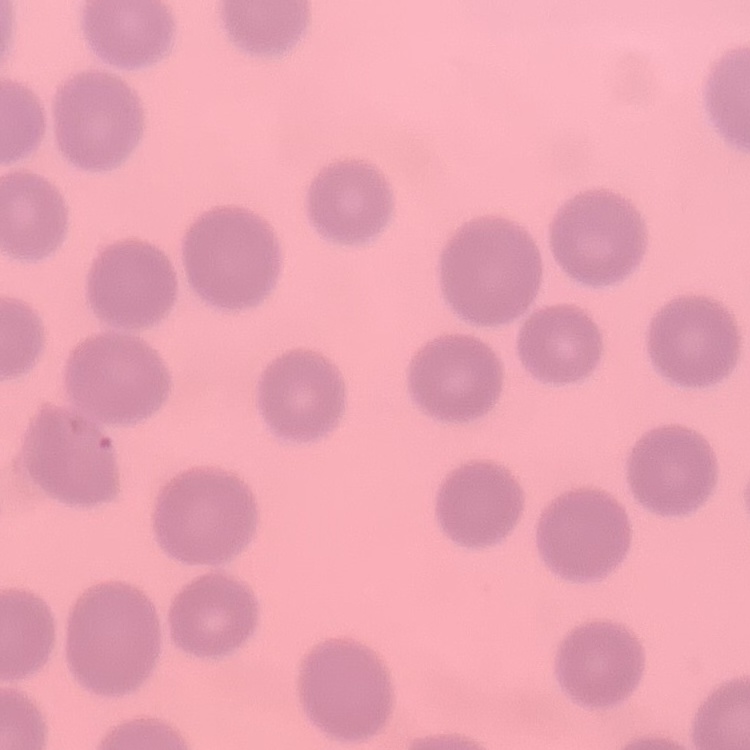

Summary:
  - Erythrocyte morphology: no rouleaux formation
  - Preparation: thin peripheral smear
  - Stain: Field's or Giemsa
  - Image type: square crop of a larger photomicrograph